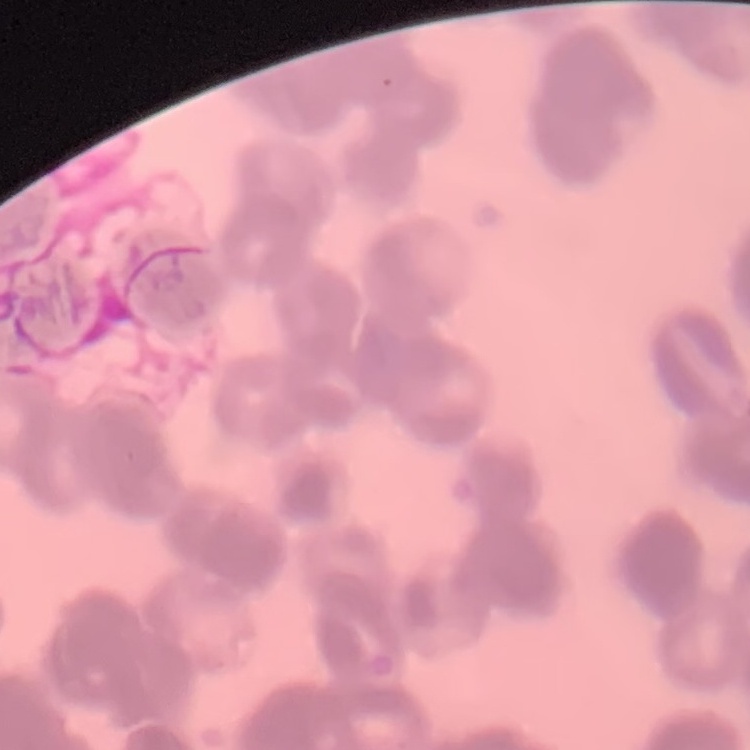
red blood cell morphology = rouleaux formation
stain = Field's or Giemsa
preparation = thin blood film
image type = square crop of a larger photomicrograph